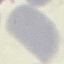
Summary:
  - Result: negative for malaria parasites
  - Stain: Giemsa
  - Capture: smartphone through the microscope eyepiece
  - Image type: cell patch, automatically extracted from a larger field of view and resized to 64 × 64 pixels
  - Preparation: thin blood smear